Identify the cell.
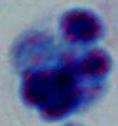
This is a leukocyte.

{
  "magnification": "1000x",
  "modality": "photomicrograph"
}